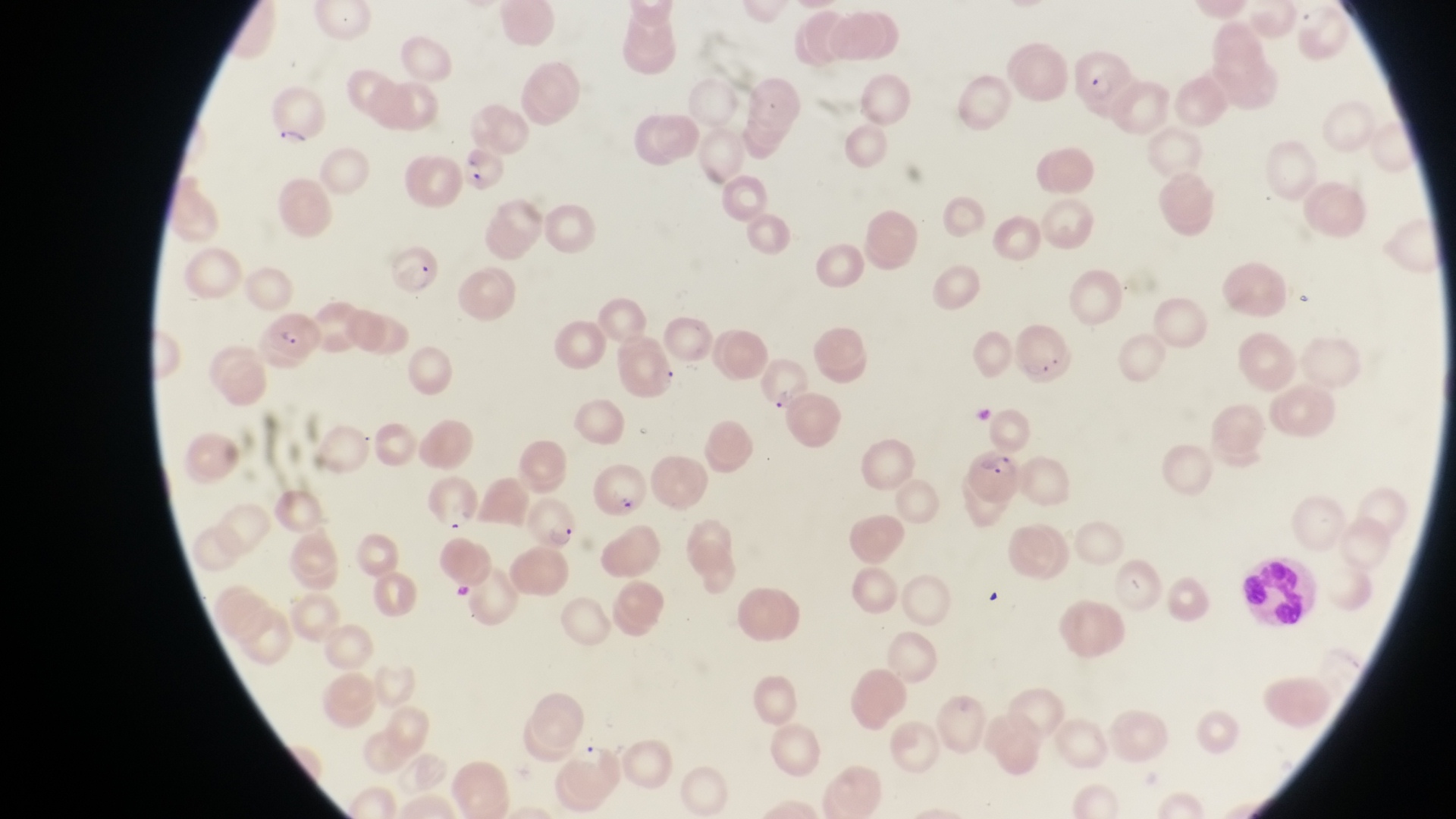
magnification = 1000x
parasitised red blood cell locations = approximate bounding boxes as {left, top, right, bottom} in pixels: {1065, 46, 1134, 117}, {264, 76, 328, 148}, {462, 149, 508, 194}, {380, 245, 446, 300}, {259, 307, 320, 370}, {968, 447, 1028, 507}
image size = 1456×819 pixels
country = Uganda
preparation = thin blood smear
capture = smartphone photograph through the eyepiece of an Olympus CX-23 microscope
field of view = single
object labeled both leukocyte and artifact (platelet-like body, stain precipitate, or debris) by the source = approximate bounding boxes as {left, top, right, bottom} in pixels: {1235, 548, 1307, 631}